Comment on the morphology of the erythrocytes.
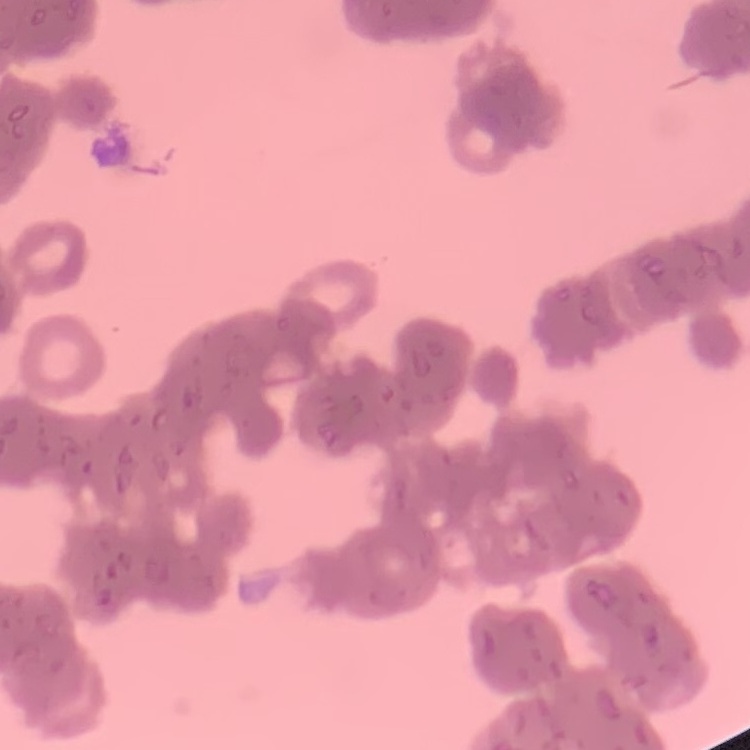
They show rouleaux formation.

Summary:
  - Stain: Field's or Giemsa
  - Preparation: thin blood film
  - Image type: one tile cut from a larger photomicrograph